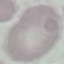

result = negative for malaria parasites
capture = smartphone through the microscope eyepiece
image type = cell patch, automatically extracted from a larger field of view and resized to 64 × 64 pixels
stain = Giemsa
preparation = thin blood film